Give the extent of all Trypanosoma brucei.
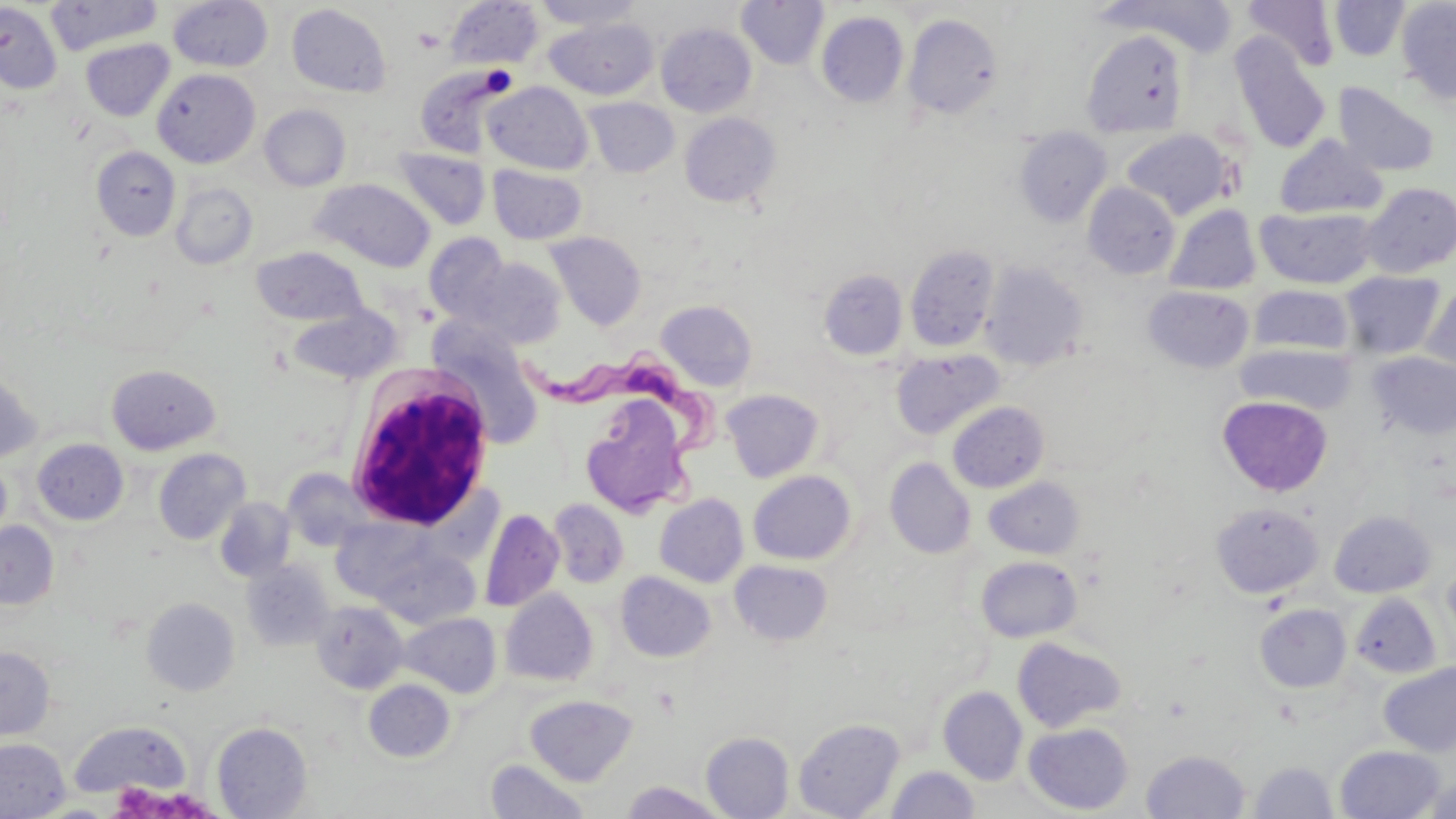
Approximate bounding boxes as (x1,y1)-(x2,y2) corner pairs in pixels.
Trypanosoma brucei: (524,345)-(725,514).

slide-level diagnosis = Trypanosoma brucei
image size = 1456×819 pixels
magnification = 1000x
field of view = one of a larger specimen
platelet locations = approximate bounding boxes as (x1,y1)-(x2,y2) corner pairs in pixels: (414,29)-(444,52)
uninfected red blood cell locations = approximate bounding boxes as (x1,y1)-(x2,y2) corner pairs in pixels: (45,0)-(163,55), (532,0)-(645,30), (736,0)-(829,69), (1329,0)-(1410,61), (1395,0)-(1456,105), (167,1)-(274,72), (445,1)-(544,70), (1104,1)-(1239,56), (1241,1)-(1340,71), (0,2)-(62,94), (286,4)-(392,97), (816,12)-(909,107), (903,13)-(1004,121), (544,17)-(658,100), (656,23)-(756,117), (1082,30)-(1189,137), (1231,37)-(1331,154), (80,38)-(174,121), (415,65)-(511,157), (152,68)-(260,168), (483,81)-(593,174), (1333,81)-(1441,177), (583,97)-(679,178), (259,104)-(350,191), (680,112)-(781,207), (1014,127)-(1112,227), (1121,128)-(1234,220), (1274,135)-(1387,219), (91,146)-(180,240), (393,147)-(491,231), (487,165)-(587,245), (311,179)-(435,272), (1360,181)-(1456,277), (170,182)-(258,269), (1083,183)-(1180,279), (1164,204)-(1260,295), (1255,206)-(1380,289), (545,232)-(646,330), (424,234)-(512,324), (905,245)-(999,352), (251,246)-(368,326), (461,256)-(566,348), (980,261)-(1088,371), (819,268)-(908,360), (1341,270)-(1445,359), (1421,283)-(1455,379), (1248,285)-(1354,357), (1144,286)-(1254,373), (656,299)-(758,391), (287,304)-(403,384), (434,334)-(546,449), (1236,344)-(1353,414), (891,349)-(1004,440), (1367,351)-(1456,441), (106,364)-(220,454), (0,371)-(41,462), (721,389)-(825,482), (1217,395)-(1334,496), (580,397)-(693,516), (947,401)-(1049,493), (33,439)-(128,525), (153,449)-(250,545), (0,457)-(12,549), (884,457)-(976,559), (282,469)-(374,551), (748,470)-(856,565), (983,476)-(1085,559), (655,493)-(749,587), (215,497)-(295,582), (548,498)-(629,588), (1211,502)-(1323,598), (480,508)-(563,612), (1329,510)-(1436,598), (0,521)-(59,609), (366,542)-(482,629), (976,555)-(1082,642), (729,559)-(834,646), (242,560)-(335,651), (1443,562)-(1456,642), (616,571)-(716,662), (500,588)-(598,687), (1349,592)-(1441,678), (142,597)-(240,696), (311,601)-(408,694), (1255,603)-(1351,693), (401,613)-(501,698), (1012,637)-(1127,733), (0,646)-(55,739), (1379,662)-(1456,756), (363,679)-(455,762), (938,686)-(1028,784), (525,695)-(637,786), (793,717)-(905,819), (68,721)-(191,799), (212,722)-(312,818), (1024,722)-(1134,814), (701,731)-(794,818), (0,738)-(69,819), (1334,745)-(1446,818), (1141,749)-(1251,819), (485,759)-(589,818), (1248,760)-(1338,819), (885,765)-(979,819), (1421,775)-(1456,819), (619,780)-(730,819)
modality = light microscopy
stain = May-Grünwald-Giemsa
white blood cell locations = approximate bounding boxes as (x1,y1)-(x2,y2) corner pairs in pixels: (345,368)-(496,534)
preparation = thin blood smear